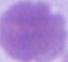
Summary:
  - Magnification: 1000x
  - Modality: micrograph
  - Identification: red blood cell